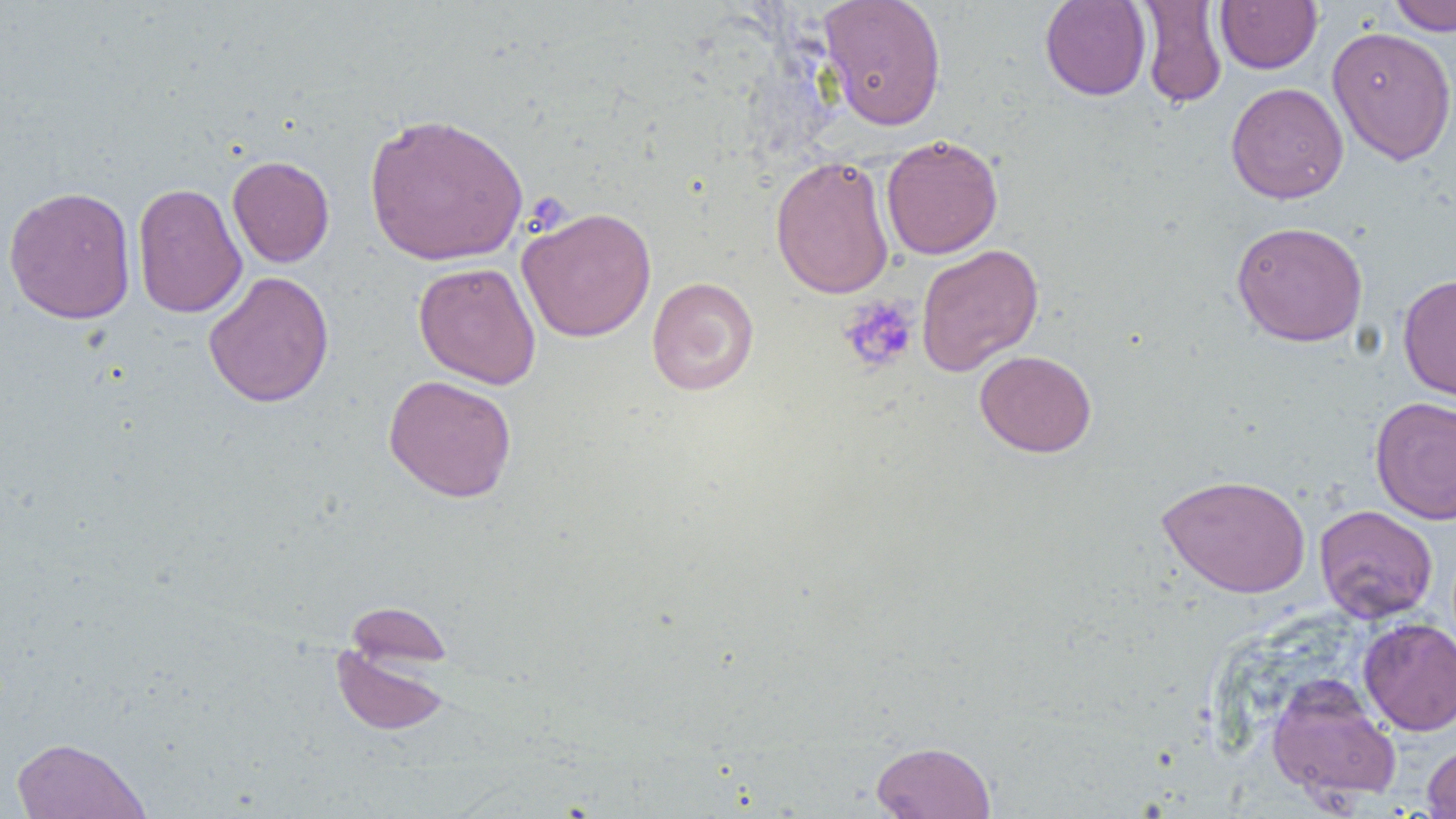

Summary:
  - Coordinate format: approximate bounding boxes as named x1/y1/x2/y2 corners in pixels
  - Platelet locations: (x1=837, y1=295, x2=920, y2=374)
  - Uninfected red blood cell locations: (x1=818, y1=0, x2=947, y2=131), (x1=1040, y1=0, x2=1152, y2=101), (x1=1386, y1=0, x2=1456, y2=35), (x1=1138, y1=1, x2=1227, y2=109), (x1=1215, y1=1, x2=1322, y2=74), (x1=1326, y1=26, x2=1456, y2=165), (x1=1225, y1=82, x2=1349, y2=204), (x1=363, y1=111, x2=529, y2=266), (x1=881, y1=134, x2=1003, y2=260), (x1=227, y1=155, x2=334, y2=268), (x1=770, y1=155, x2=895, y2=299), (x1=132, y1=182, x2=247, y2=319), (x1=3, y1=185, x2=137, y2=325), (x1=517, y1=206, x2=657, y2=342), (x1=1231, y1=221, x2=1368, y2=347), (x1=915, y1=243, x2=1044, y2=376), (x1=413, y1=261, x2=541, y2=389), (x1=203, y1=271, x2=334, y2=408), (x1=1397, y1=273, x2=1456, y2=404), (x1=646, y1=277, x2=759, y2=396), (x1=974, y1=350, x2=1097, y2=458), (x1=383, y1=374, x2=518, y2=503), (x1=1370, y1=396, x2=1456, y2=525), (x1=1157, y1=473, x2=1311, y2=597), (x1=1314, y1=504, x2=1438, y2=623), (x1=344, y1=600, x2=453, y2=673), (x1=1359, y1=618, x2=1456, y2=735), (x1=330, y1=638, x2=452, y2=736), (x1=1267, y1=675, x2=1402, y2=806), (x1=11, y1=736, x2=151, y2=818), (x1=871, y1=740, x2=996, y2=818), (x1=1422, y1=743, x2=1456, y2=818)
  - Slide-level diagnosis: no evidence of blood parasites
  - Magnification: 1000x
  - Preparation: thin blood smear
  - Field of view: one of a larger specimen
  - Image size: 1456×819 pixels
  - Modality: optical microscopy